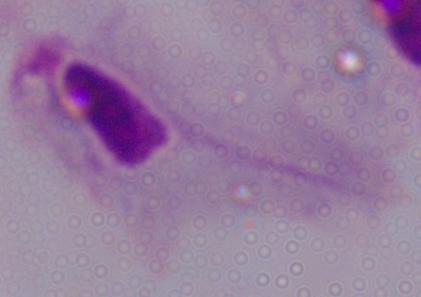

modality = micrograph
identification = trichomonad
magnification = 1000x